Comment on the morphology of the erythrocytes.
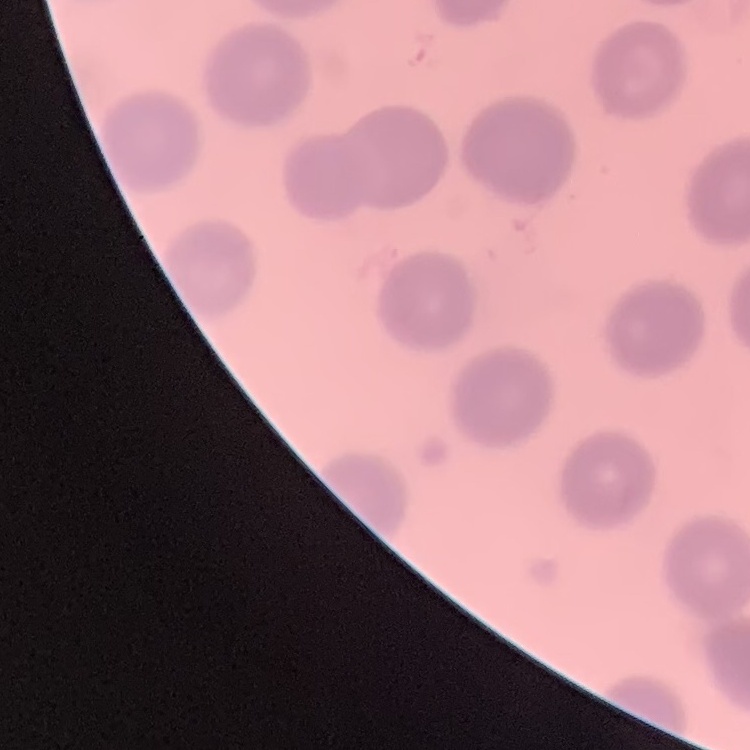

They show no rouleaux formation.

Summary:
  - Stain: Field's or Giemsa
  - Preparation: thin blood film
  - Image type: square crop of a larger photomicrograph